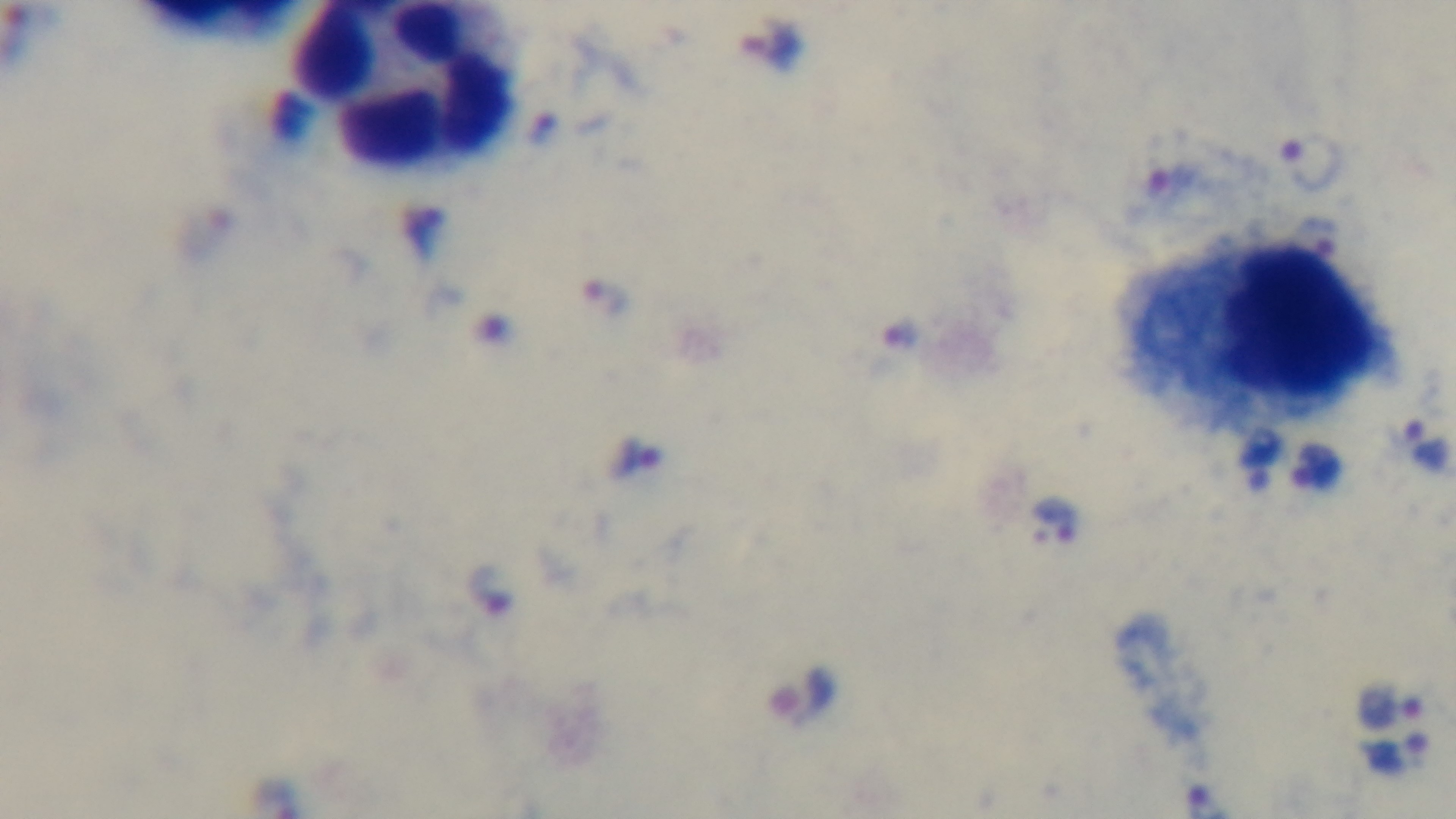

preparation: thick
stain: Giemsa
objective: 100x oil immersion
capture: mounted 4K digital camera
malaria_status: infected
modality: light microscopy
field_of_view: single